Report the malaria status of this cell.
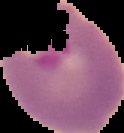
Parasitized.

image type = segmented cell region with the area outside set to black
image size = 124×133 pixels
preparation = thin blood smear